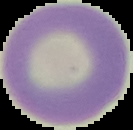
preparation = thin blood smear
image size = 133×130 pixels
result = no malaria parasites seen
image type = segmented cell region with the area outside set to black